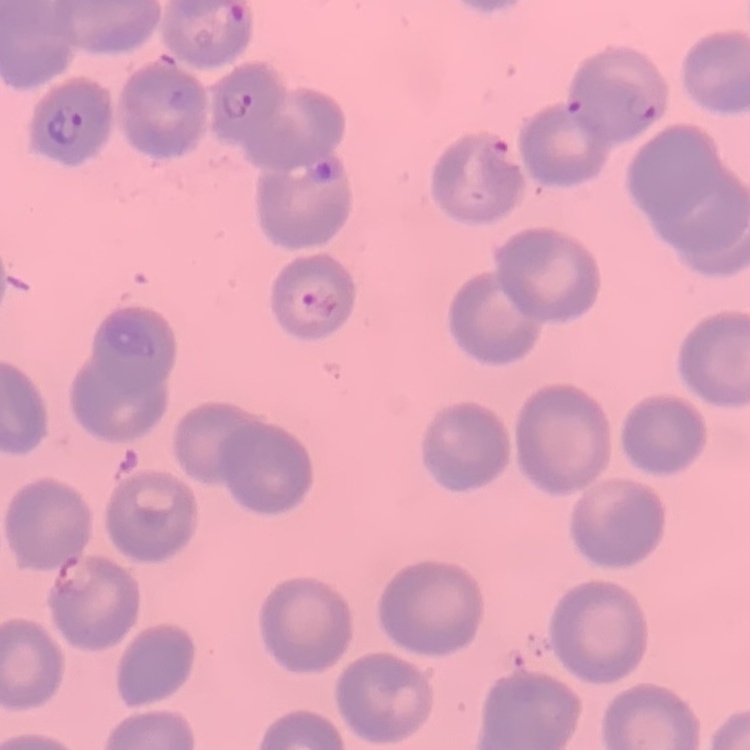

red blood cell morphology = no rouleaux formation
stain = Field's or Giemsa
image type = one tile cut from a larger photomicrograph
preparation = thin blood smear